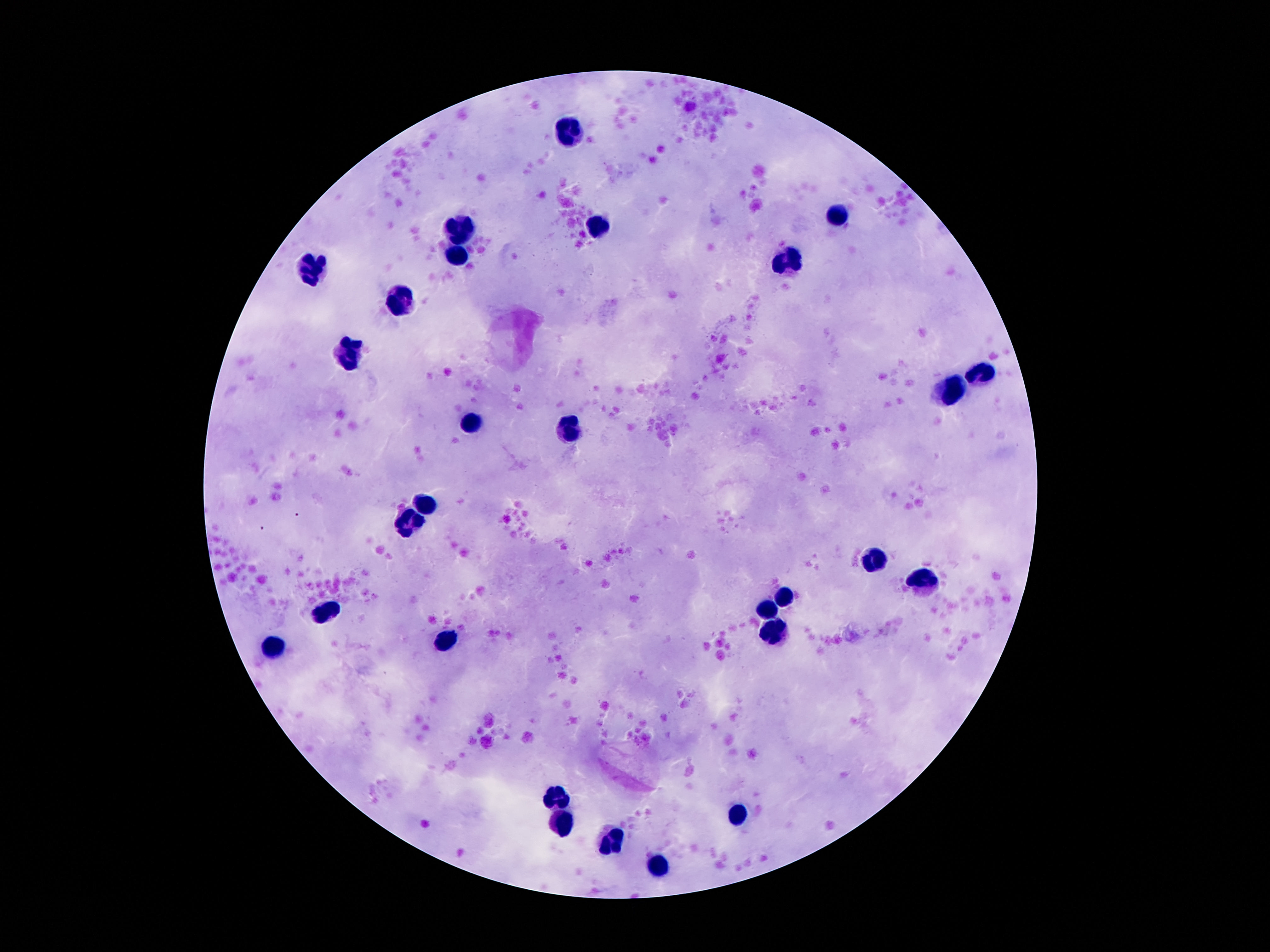
Approximate centers as (x, y) in pixels.
Summary:
  - Leukocyte locations: (571, 135), (836, 216), (464, 225), (598, 225), (457, 257), (791, 261), (310, 269), (399, 299), (350, 356), (980, 370), (949, 391), (470, 423), (571, 430), (426, 504), (409, 525), (875, 561), (926, 582), (785, 592), (766, 610), (325, 611), (770, 632), (447, 638), (272, 646), (558, 798), (739, 816), (560, 825), (613, 841), (661, 863)
  - Field of view: one from this slide
  - Capture: smartphone camera through the microscope eyepiece
  - Stain: Giemsa
  - Preparation: thick blood smear
  - Patient malaria status: uninfected
  - Image size: 1270×952 pixels
  - Magnification: 100x